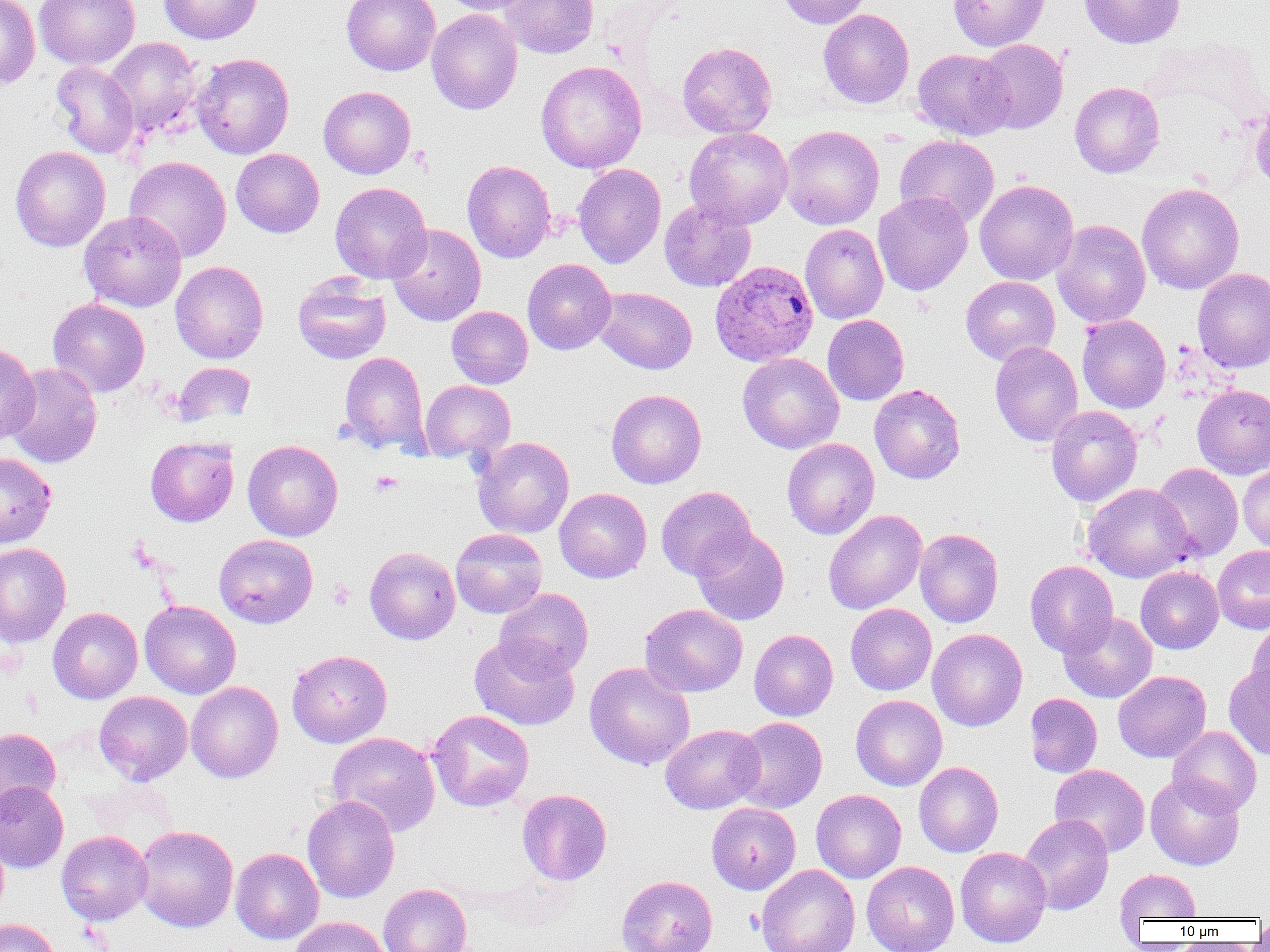

Approximate bounding boxes as named x1/y1/x2/y2 corners in pixels. Uninfected red blood cell locations: (x1=34, y1=0, x2=140, y2=70), (x1=158, y1=0, x2=263, y2=45), (x1=341, y1=0, x2=441, y2=76), (x1=438, y1=0, x2=539, y2=15), (x1=500, y1=0, x2=600, y2=59), (x1=776, y1=0, x2=871, y2=28), (x1=948, y1=0, x2=1050, y2=51), (x1=1078, y1=0, x2=1185, y2=49), (x1=0, y1=1, x2=40, y2=89), (x1=818, y1=8, x2=914, y2=108), (x1=426, y1=9, x2=523, y2=114), (x1=104, y1=37, x2=204, y2=138), (x1=975, y1=39, x2=1068, y2=134), (x1=677, y1=41, x2=777, y2=138), (x1=912, y1=48, x2=1014, y2=140), (x1=192, y1=53, x2=294, y2=159), (x1=536, y1=60, x2=647, y2=173), (x1=50, y1=61, x2=139, y2=159), (x1=1070, y1=82, x2=1164, y2=178), (x1=318, y1=86, x2=416, y2=179), (x1=1249, y1=100, x2=1270, y2=191), (x1=780, y1=125, x2=884, y2=230), (x1=683, y1=127, x2=793, y2=229), (x1=894, y1=134, x2=999, y2=229), (x1=10, y1=146, x2=110, y2=252), (x1=231, y1=148, x2=324, y2=237), (x1=124, y1=156, x2=231, y2=263), (x1=462, y1=160, x2=556, y2=263), (x1=573, y1=163, x2=666, y2=268), (x1=974, y1=179, x2=1078, y2=285), (x1=330, y1=182, x2=431, y2=283), (x1=1137, y1=182, x2=1244, y2=295), (x1=872, y1=192, x2=973, y2=296), (x1=659, y1=199, x2=756, y2=292), (x1=78, y1=210, x2=187, y2=312), (x1=1052, y1=220, x2=1151, y2=328), (x1=386, y1=223, x2=486, y2=326), (x1=800, y1=223, x2=889, y2=324), (x1=522, y1=258, x2=616, y2=355), (x1=170, y1=261, x2=268, y2=363), (x1=1192, y1=267, x2=1270, y2=373), (x1=292, y1=274, x2=391, y2=364), (x1=960, y1=276, x2=1060, y2=366), (x1=595, y1=286, x2=697, y2=374), (x1=47, y1=298, x2=150, y2=396), (x1=446, y1=305, x2=533, y2=389), (x1=822, y1=314, x2=909, y2=405), (x1=1077, y1=315, x2=1171, y2=413), (x1=989, y1=341, x2=1083, y2=446), (x1=0, y1=342, x2=40, y2=445), (x1=338, y1=351, x2=430, y2=455), (x1=737, y1=353, x2=844, y2=454), (x1=172, y1=362, x2=255, y2=427), (x1=4, y1=363, x2=102, y2=468), (x1=420, y1=380, x2=516, y2=463), (x1=869, y1=383, x2=965, y2=484), (x1=1192, y1=384, x2=1270, y2=478), (x1=606, y1=389, x2=706, y2=489), (x1=1046, y1=405, x2=1142, y2=507), (x1=472, y1=436, x2=574, y2=538), (x1=145, y1=437, x2=238, y2=527), (x1=781, y1=438, x2=880, y2=539), (x1=243, y1=440, x2=343, y2=541), (x1=0, y1=453, x2=56, y2=548), (x1=1237, y1=462, x2=1270, y2=552), (x1=1152, y1=463, x2=1243, y2=562), (x1=1083, y1=483, x2=1195, y2=582), (x1=655, y1=486, x2=756, y2=580), (x1=554, y1=488, x2=652, y2=583), (x1=823, y1=510, x2=927, y2=614), (x1=690, y1=527, x2=789, y2=625), (x1=914, y1=527, x2=1004, y2=628), (x1=450, y1=528, x2=547, y2=618), (x1=214, y1=534, x2=318, y2=628), (x1=0, y1=542, x2=72, y2=648), (x1=1212, y1=545, x2=1270, y2=633), (x1=364, y1=546, x2=461, y2=644), (x1=1025, y1=560, x2=1118, y2=657), (x1=1135, y1=566, x2=1224, y2=654), (x1=494, y1=588, x2=593, y2=680), (x1=139, y1=600, x2=241, y2=699), (x1=640, y1=603, x2=748, y2=697), (x1=845, y1=603, x2=937, y2=695), (x1=47, y1=607, x2=143, y2=704), (x1=1059, y1=612, x2=1157, y2=703), (x1=1247, y1=620, x2=1270, y2=713), (x1=927, y1=628, x2=1028, y2=731), (x1=749, y1=629, x2=838, y2=721), (x1=469, y1=636, x2=580, y2=731), (x1=286, y1=649, x2=392, y2=748), (x1=584, y1=662, x2=695, y2=770), (x1=1224, y1=665, x2=1270, y2=761), (x1=1113, y1=671, x2=1211, y2=763), (x1=186, y1=681, x2=283, y2=783), (x1=94, y1=691, x2=192, y2=785), (x1=1024, y1=693, x2=1102, y2=778), (x1=851, y1=694, x2=947, y2=790), (x1=427, y1=709, x2=534, y2=811), (x1=731, y1=717, x2=827, y2=813), (x1=660, y1=724, x2=764, y2=814), (x1=1168, y1=725, x2=1262, y2=816), (x1=0, y1=727, x2=61, y2=817), (x1=326, y1=731, x2=441, y2=837), (x1=914, y1=762, x2=1003, y2=857), (x1=1050, y1=764, x2=1150, y2=857), (x1=1145, y1=774, x2=1245, y2=871), (x1=0, y1=781, x2=69, y2=873), (x1=517, y1=789, x2=612, y2=886), (x1=811, y1=789, x2=906, y2=883), (x1=302, y1=795, x2=399, y2=903), (x1=706, y1=803, x2=801, y2=894), (x1=1019, y1=814, x2=1114, y2=915), (x1=134, y1=825, x2=238, y2=932), (x1=56, y1=830, x2=153, y2=925), (x1=956, y1=846, x2=1051, y2=947), (x1=230, y1=847, x2=324, y2=944), (x1=861, y1=861, x2=960, y2=952), (x1=756, y1=863, x2=860, y2=952), (x1=1115, y1=869, x2=1201, y2=922), (x1=616, y1=875, x2=718, y2=952), (x1=378, y1=883, x2=473, y2=952), (x1=288, y1=916, x2=388, y2=952), (x1=0, y1=918, x2=61, y2=952), (x1=1253, y1=918, x2=1270, y2=943). Platelet locations: (x1=409, y1=145, x2=433, y2=175), (x1=370, y1=471, x2=403, y2=497), (x1=328, y1=580, x2=355, y2=610). Plasmodium ovale-infected red blood cell locations: (x1=710, y1=260, x2=818, y2=366). Slide-level diagnosis: Plasmodium ovale. Single field of view. 1000x magnification. Image is 1270×952 pixels. Light microscopy. Thin blood smear.